Identify the blood parasite species.
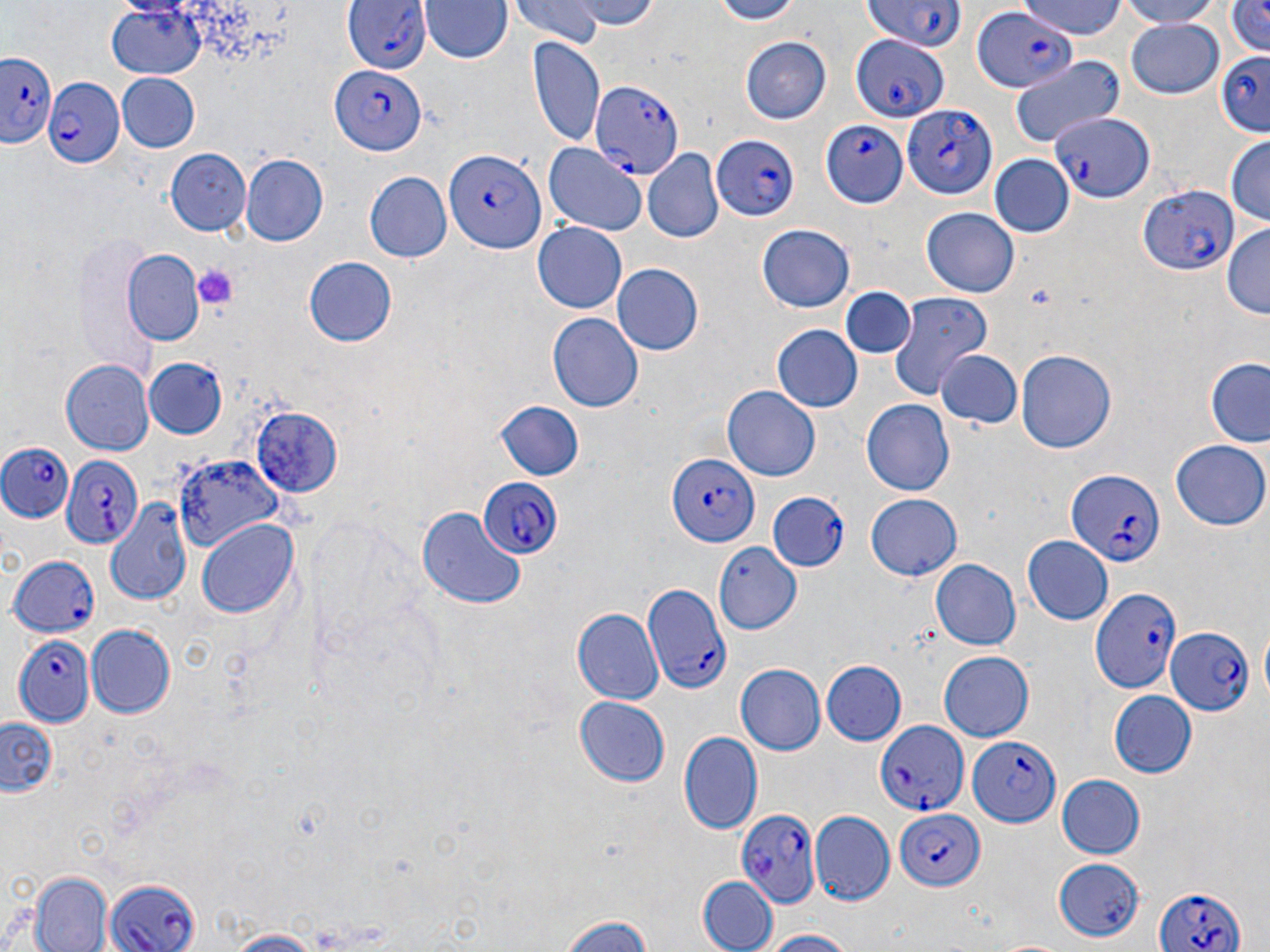
Plasmodium falciparum.

{
  "platelet_locations": "approximate bounding boxes as [x1, y1, x2, y2] in pixels: [191, 264, 239, 311]",
  "image_size": "1270×952 pixels",
  "uninfected_red_blood_cell_locations": "approximate bounding boxes as [x1, y1, x2, y2] in pixels: [564, 0, 664, 27], [700, 0, 809, 25], [1021, 0, 1127, 40], [1110, 0, 1226, 27], [1222, 0, 1270, 56], [420, 1, 511, 64], [509, 1, 605, 49], [105, 3, 207, 80], [1122, 17, 1225, 100], [740, 32, 833, 123], [526, 38, 606, 150], [1009, 54, 1127, 145], [117, 74, 200, 152], [1224, 137, 1269, 227], [543, 142, 647, 235], [166, 148, 251, 236], [644, 150, 723, 243], [989, 154, 1072, 238], [240, 155, 328, 245], [363, 170, 450, 264], [920, 209, 1021, 297], [532, 219, 627, 312], [757, 222, 853, 311], [1221, 223, 1269, 318], [122, 251, 206, 344], [303, 257, 398, 345], [613, 263, 703, 355], [842, 288, 912, 360], [888, 293, 993, 400], [547, 313, 643, 413], [773, 325, 862, 414], [1017, 348, 1118, 454], [933, 350, 1023, 431], [141, 357, 228, 440], [60, 359, 152, 455], [1208, 360, 1270, 448], [722, 386, 820, 481], [491, 401, 583, 481], [861, 401, 955, 495], [1171, 440, 1268, 531], [175, 455, 285, 555], [865, 494, 963, 581], [105, 501, 194, 609], [417, 506, 526, 610], [198, 519, 298, 621], [1022, 537, 1112, 623], [714, 544, 802, 634], [930, 559, 1021, 650], [573, 607, 662, 705], [86, 624, 176, 718], [937, 650, 1035, 742], [821, 660, 907, 744], [737, 664, 826, 754], [1108, 691, 1196, 778], [575, 698, 670, 786], [0, 719, 57, 798], [678, 730, 763, 835], [1056, 774, 1145, 859], [808, 812, 893, 904], [1051, 855, 1149, 944], [26, 872, 114, 952], [698, 875, 777, 951], [553, 912, 661, 952], [222, 929, 323, 951], [758, 930, 857, 952]",
  "magnification": "1000x",
  "modality": "optical microscopy",
  "field_of_view": "one of a larger specimen",
  "preparation": "thin blood film",
  "plasmodium_falciparum_infected_red_blood_cell_locations": "approximate bounding boxes as [x1, y1, x2, y2] in pixels: [342, 0, 434, 76], [863, 0, 967, 50], [972, 7, 1077, 95], [849, 32, 947, 122], [1, 50, 57, 150], [1216, 50, 1270, 140], [331, 67, 425, 154], [45, 76, 126, 169], [592, 80, 687, 176], [902, 105, 996, 200], [1052, 108, 1153, 202], [821, 122, 910, 203], [710, 132, 800, 223], [444, 146, 545, 252], [1137, 184, 1236, 276], [0, 442, 76, 525], [667, 453, 760, 546], [59, 456, 145, 550], [1066, 469, 1165, 571], [474, 479, 561, 560], [769, 491, 850, 572], [6, 551, 103, 644], [641, 585, 731, 698], [1090, 589, 1179, 696], [1164, 627, 1255, 717], [12, 634, 95, 726], [875, 720, 970, 813], [967, 733, 1060, 827], [738, 809, 818, 907], [894, 810, 984, 890], [105, 878, 197, 952], [1153, 885, 1245, 952]",
  "stain": "May-Grünwald-Giemsa"
}